Assess this cell for malaria.
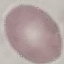

Uninfected.

Photographed with a smartphone camera at the microscope eyepiece. Cell patch, automatically extracted from a larger field of view and resized to 64 × 64 pixels. Thin blood film. Giemsa-stained preparation.